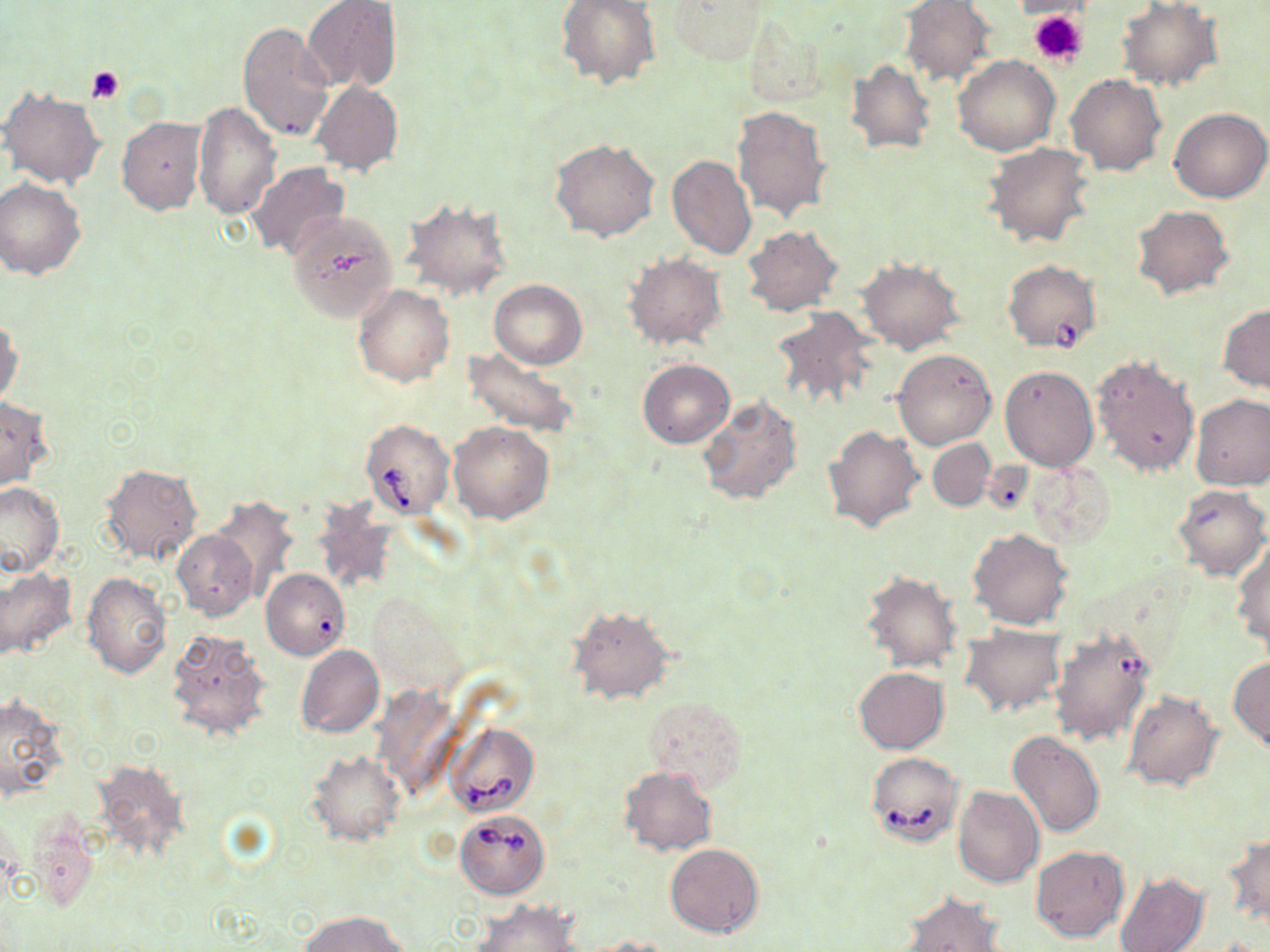 Approximate bounding boxes as (x1,y1)-(x2,y2) corner pairs in pixels. Babesia divergens-infected red blood cell locations: (1002,263)-(1098,355), (360,418)-(453,518), (443,721)-(539,819), (865,751)-(964,845), (454,810)-(549,899). Uninfected red blood cell locations: (557,0)-(661,91), (665,0)-(768,66), (303,1)-(402,93), (901,1)-(995,85), (1117,1)-(1221,90), (741,9)-(831,103), (237,22)-(336,143), (953,55)-(1060,156), (846,58)-(936,154), (1066,74)-(1166,175), (310,80)-(403,177), (0,85)-(106,189), (192,101)-(281,220), (733,105)-(831,224), (1168,107)-(1269,203), (117,117)-(208,215), (550,138)-(660,242), (982,142)-(1094,248), (667,155)-(757,260), (246,163)-(350,262), (0,177)-(88,279), (400,196)-(513,300), (1132,205)-(1233,298), (287,210)-(398,323), (743,225)-(842,316), (624,253)-(728,351), (856,258)-(966,354), (489,279)-(587,368), (353,284)-(456,387), (1218,304)-(1270,393), (770,306)-(881,416), (0,316)-(22,408), (464,347)-(578,437), (893,348)-(996,450), (1092,353)-(1201,479), (638,359)-(735,449), (1000,364)-(1099,471), (696,393)-(804,507), (1191,393)-(1270,490), (0,396)-(54,489), (448,421)-(554,524), (823,425)-(924,532), (928,438)-(995,511), (1024,460)-(1115,547), (98,462)-(203,566), (0,481)-(64,577), (1169,483)-(1269,580), (209,496)-(299,599), (311,500)-(402,597), (968,529)-(1075,629), (173,530)-(258,620), (1232,542)-(1270,652), (0,567)-(75,661), (261,568)-(350,661), (860,569)-(963,673), (81,573)-(173,680), (567,605)-(674,704), (959,625)-(1065,716), (165,628)-(274,744), (1049,628)-(1156,747), (296,644)-(384,739), (1228,657)-(1270,751), (853,667)-(950,753), (1122,689)-(1222,791), (0,693)-(68,802), (641,697)-(744,788), (1008,730)-(1105,837), (307,751)-(404,847), (89,757)-(190,859), (619,767)-(717,855), (952,786)-(1045,887), (23,821)-(100,915), (1225,832)-(1269,927), (665,843)-(764,937), (1030,845)-(1129,942), (1114,873)-(1208,952), (898,891)-(1008,951), (472,901)-(584,952), (299,911)-(410,952), (583,936)-(676,951). Platelet locations: (1029,9)-(1087,67), (87,65)-(125,103). Slide-level diagnosis: Babesia divergens. Light microscopy. Image is 1270×952 pixels. Captured at 1000x magnification. One field of a larger specimen. May-Grünwald-Giemsa stain. Thin blood film.